State which cell type is depicted.
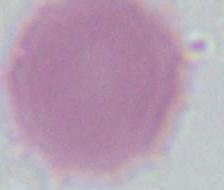

An erythrocyte.

1000x magnification. Micrograph.